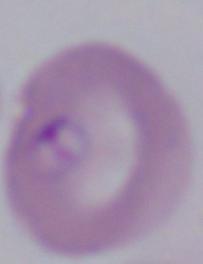
Micrograph. 1000x magnification. A Babesia parasite is seen.